Assess the morphology of the erythrocytes.
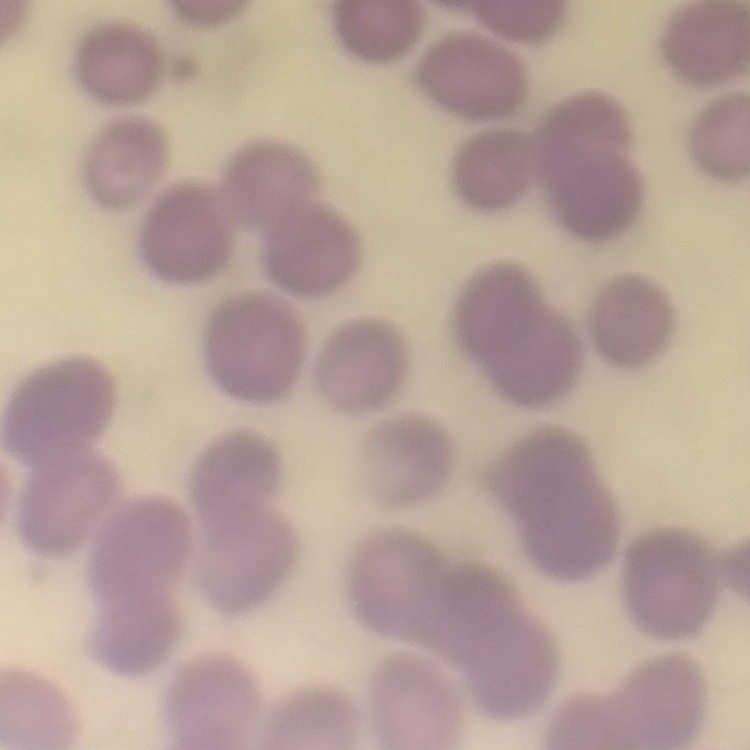
No rouleaux formation.

image type = square crop of a larger photomicrograph
stain = Field's or Giemsa
preparation = thin blood smear